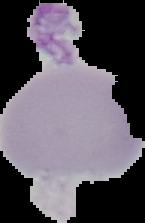

preparation = thin blood smear
malaria status = uninfected
image type = segmented cell region with the area outside set to black
image size = 145×223 pixels